Assess for Plasmodium parasites.
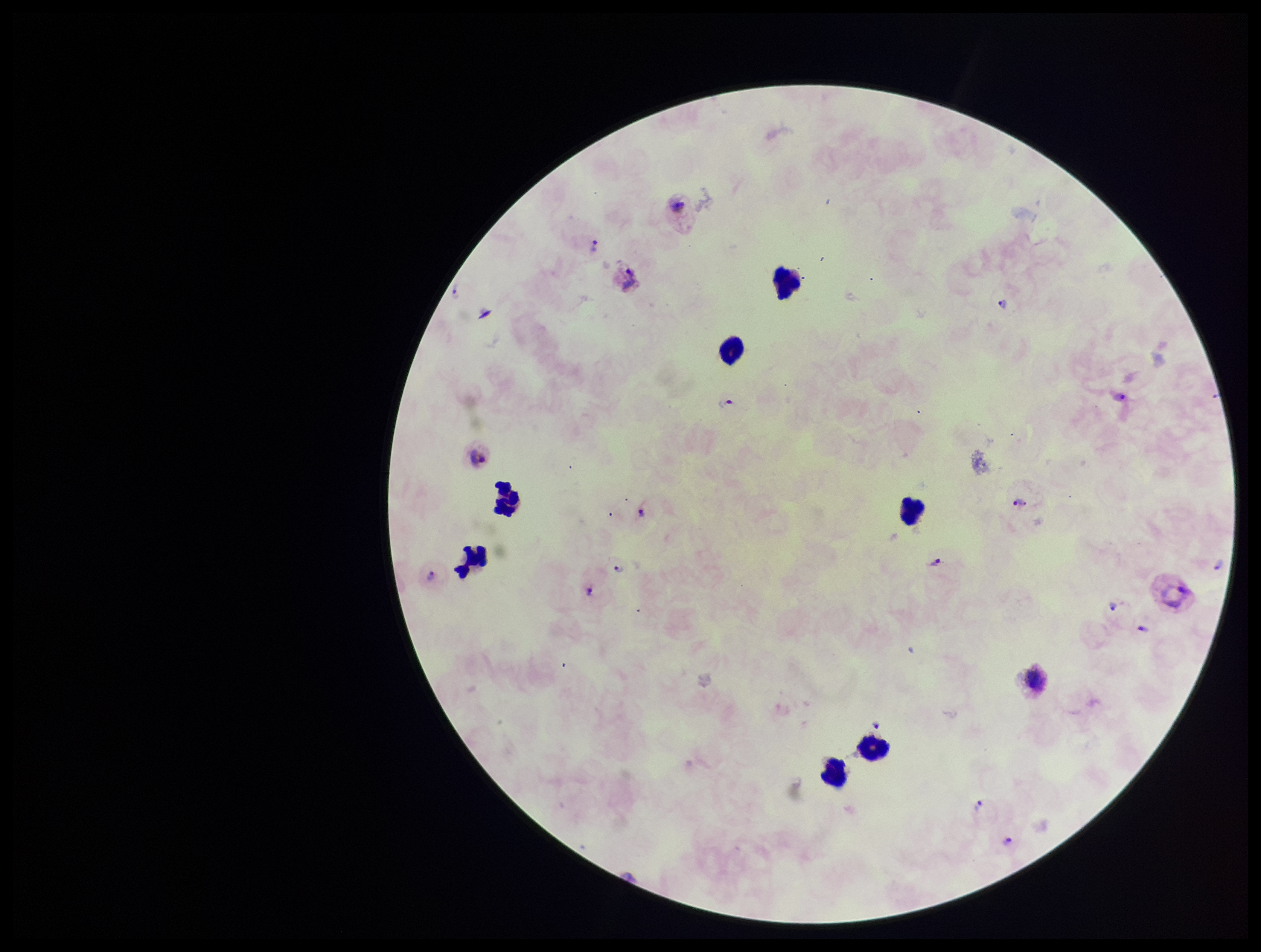
Seen.

Preparation: thick smear. Photographed through the microscope eyepiece with a smartphone camera. Leukocyte count: 8. One field from this slide. Species reported for this patient: Plasmodium vivax. Patient malaria status: infected. Image is 1261×952 pixels. Stained with Giemsa. Parasite count: 14.